Assess the morphology of the red blood cells.
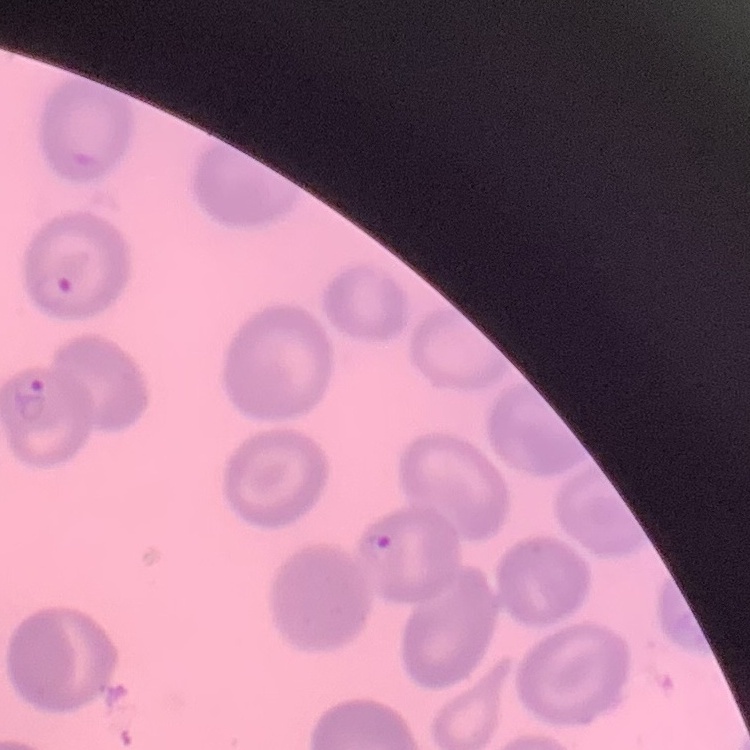
No rouleaux formation.

Thin peripheral smear. Square crop of a larger photomicrograph. Stained with either Field's or Giemsa.